Assess this cell for malaria.
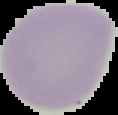
It is uninfected.

{
  "image_size": "118×115 pixels",
  "image_type": "segmented cell region with the area outside set to black",
  "preparation": "thin blood smear"
}